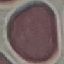
Summary:
  - Malaria status: uninfected
  - Stain: Giemsa
  - Preparation: thin blood film
  - Image type: automatically extracted cell patch, resized to 64 × 64 pixels
  - Capture: smartphone camera at the microscope eyepiece